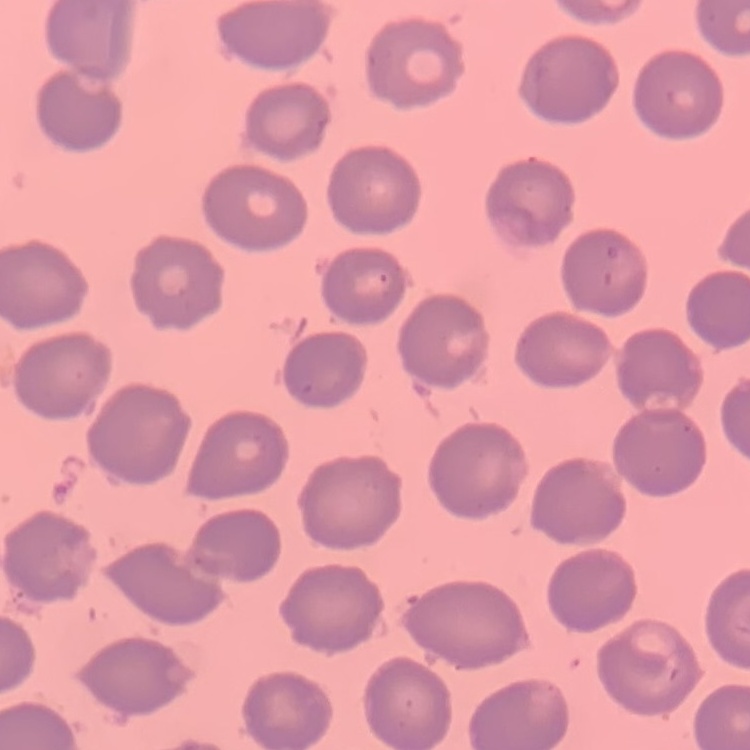
Summary:
  - Erythrocyte morphology: no rouleaux formation
  - Image type: one tile cut from a larger photomicrograph
  - Stain: Field's or Giemsa
  - Preparation: thin peripheral smear